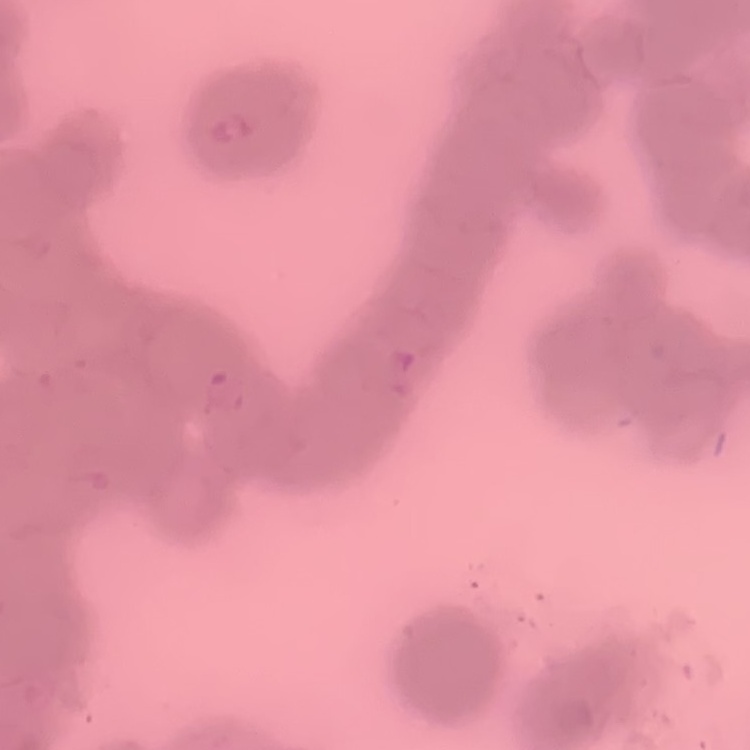
red blood cell morphology = rouleaux formation
stain = Field's or Giemsa
image type = one tile cut from a larger photomicrograph
preparation = thin blood film